Classify this cell by malaria status.
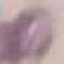

It is uninfected.

Summary:
  - Stain: Giemsa
  - Image type: cell patch, automatically extracted from a larger field of view and resized to 64 × 64 pixels
  - Preparation: thin blood smear
  - Capture: smartphone camera at the microscope eyepiece